State the preparation type.
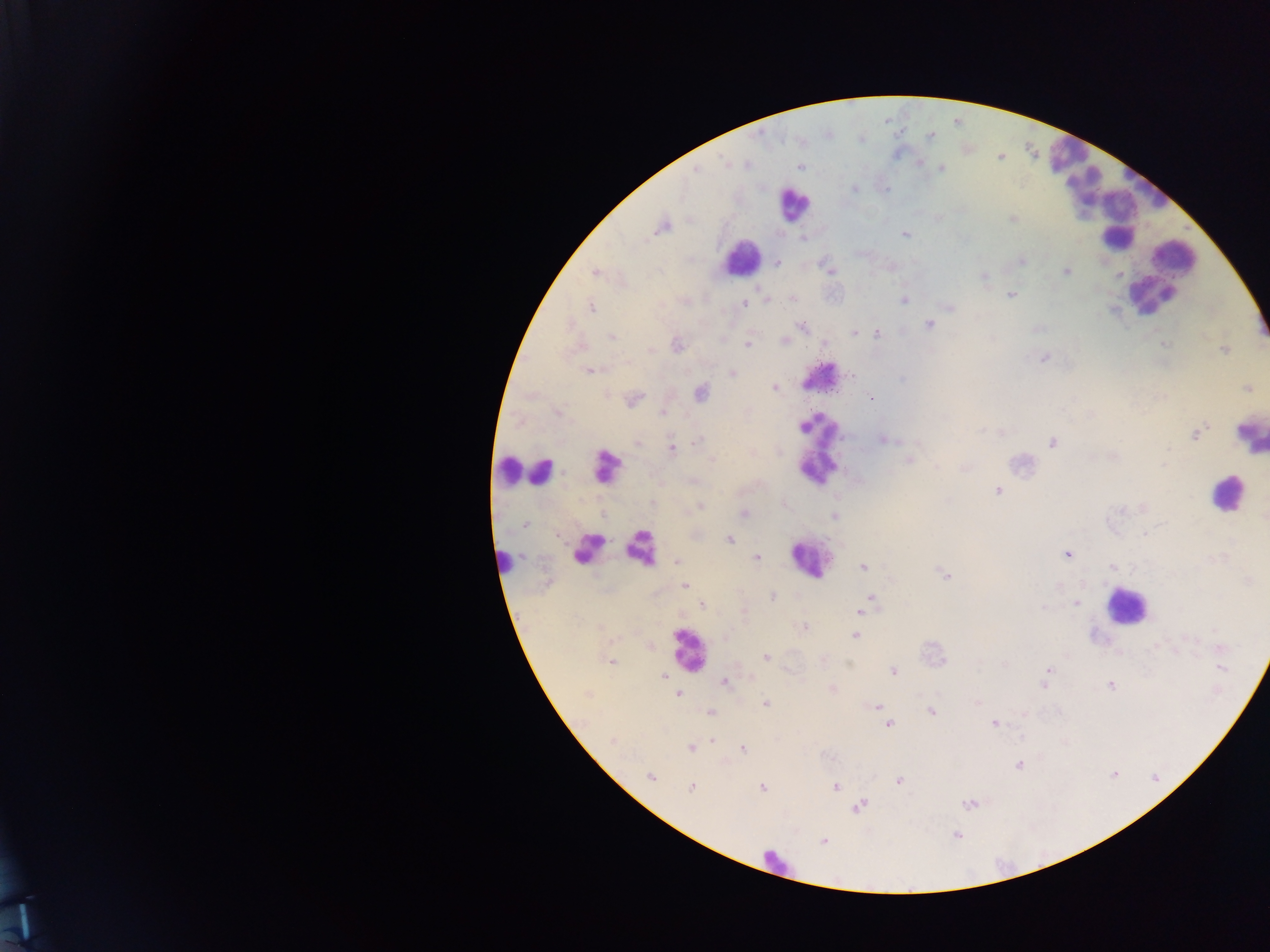

Thick blood smear.

Approximate centers as (x, y) in pixels. Malaria parasite locations: (931, 136), (919, 163), (801, 167), (939, 168), (695, 170), (853, 190), (1012, 218), (662, 227), (905, 234), (803, 237), (1020, 260), (776, 263), (891, 266), (595, 271), (829, 271), (1067, 271), (1118, 274), (983, 276), (1010, 295), (790, 298), (766, 299), (903, 299), (742, 305), (590, 306), (948, 306), (929, 323), (802, 326), (1036, 328), (854, 333), (877, 334), (611, 337), (784, 340), (1163, 344), (676, 345), (748, 345), (1225, 349), (1043, 358), (589, 371), (732, 373), (850, 376), (773, 387), (1248, 388), (700, 392), (633, 400), (871, 400), (663, 412), (1002, 432), (1196, 434), (883, 438), (698, 441), (639, 442), (1052, 442), (670, 449), (909, 460), (963, 468), (998, 485), (997, 490), (653, 504), (783, 505), (701, 506), (743, 514), (835, 516), (525, 524), (558, 534), (1146, 534), (729, 540), (1067, 554), (757, 558), (677, 561), (862, 566), (1112, 567), (945, 574), (684, 585), (772, 596), (869, 598), (1076, 603), (702, 605), (868, 605), (743, 611), (861, 612), (804, 627), (855, 635), (724, 638), (765, 657), (610, 661), (1004, 663), (1049, 669), (1220, 669), (893, 670), (663, 676), (724, 681), (1110, 685), (1043, 686), (832, 689), (677, 693), (977, 702), (765, 703), (877, 707), (931, 710), (710, 712), (994, 723), (888, 724), (711, 740), (613, 742), (691, 748), (742, 748), (1019, 764), (1113, 774), (651, 776), (899, 780), (835, 787), (691, 788), (762, 788), (968, 803), (859, 806), (956, 834), (823, 840). Leukocyte locations: (1066, 155), (1085, 181), (792, 204), (1109, 207), (1115, 217), (1143, 244), (1172, 257), (741, 258), (1162, 272), (1152, 292), (820, 376), (1249, 434), (816, 449), (1022, 464), (607, 466), (512, 470), (540, 471), (1226, 493), (640, 548), (589, 549), (811, 558), (502, 561), (1125, 605), (687, 649), (775, 862). One field of view. Image is 1270×952 pixels. Photographed through a microscope with a mobile-phone camera. Collected in Ghana.